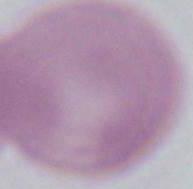

magnification = 1000x
identification = red blood cell
modality = photomicrograph